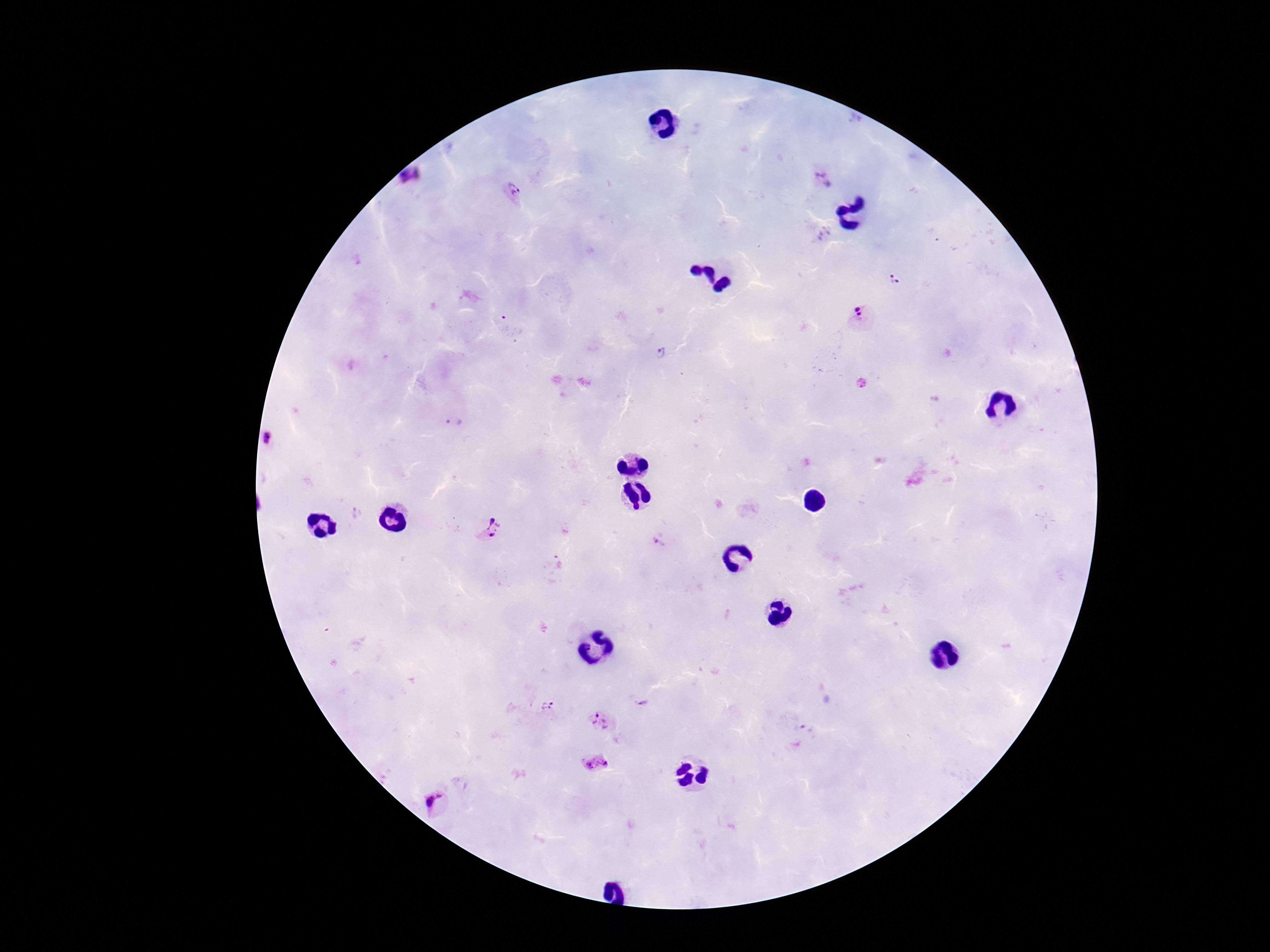 Approximate object centers, in pixels from the top-left corner. Plasmodium parasite locations: (x=411, y=178), (x=822, y=180), (x=512, y=189), (x=894, y=278), (x=862, y=318), (x=661, y=353), (x=455, y=422), (x=267, y=439), (x=489, y=529), (x=658, y=543), (x=546, y=707), (x=604, y=722), (x=597, y=765), (x=437, y=803). Image is 1270×952 pixels. Thick peripheral-blood smear. Patient malaria status: positive. One field from this slide. 100x magnification. Photographed through the microscope eyepiece with a smartphone camera. Giemsa stain.